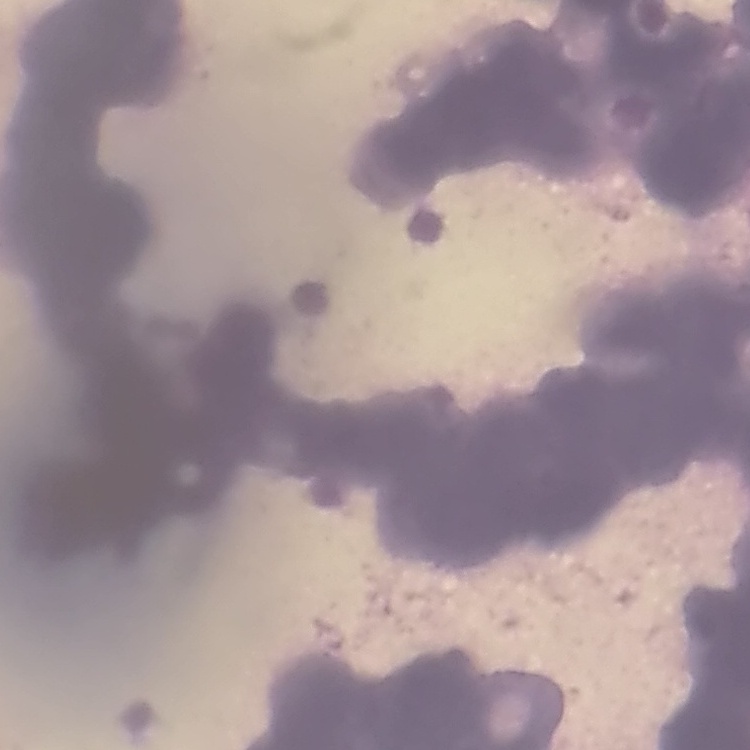

red blood cell morphology = rouleaux formation
image type = one tile cut from a larger photomicrograph
stain = Field's or Giemsa
preparation = thin blood smear